Outline each blood parasite and name the species.
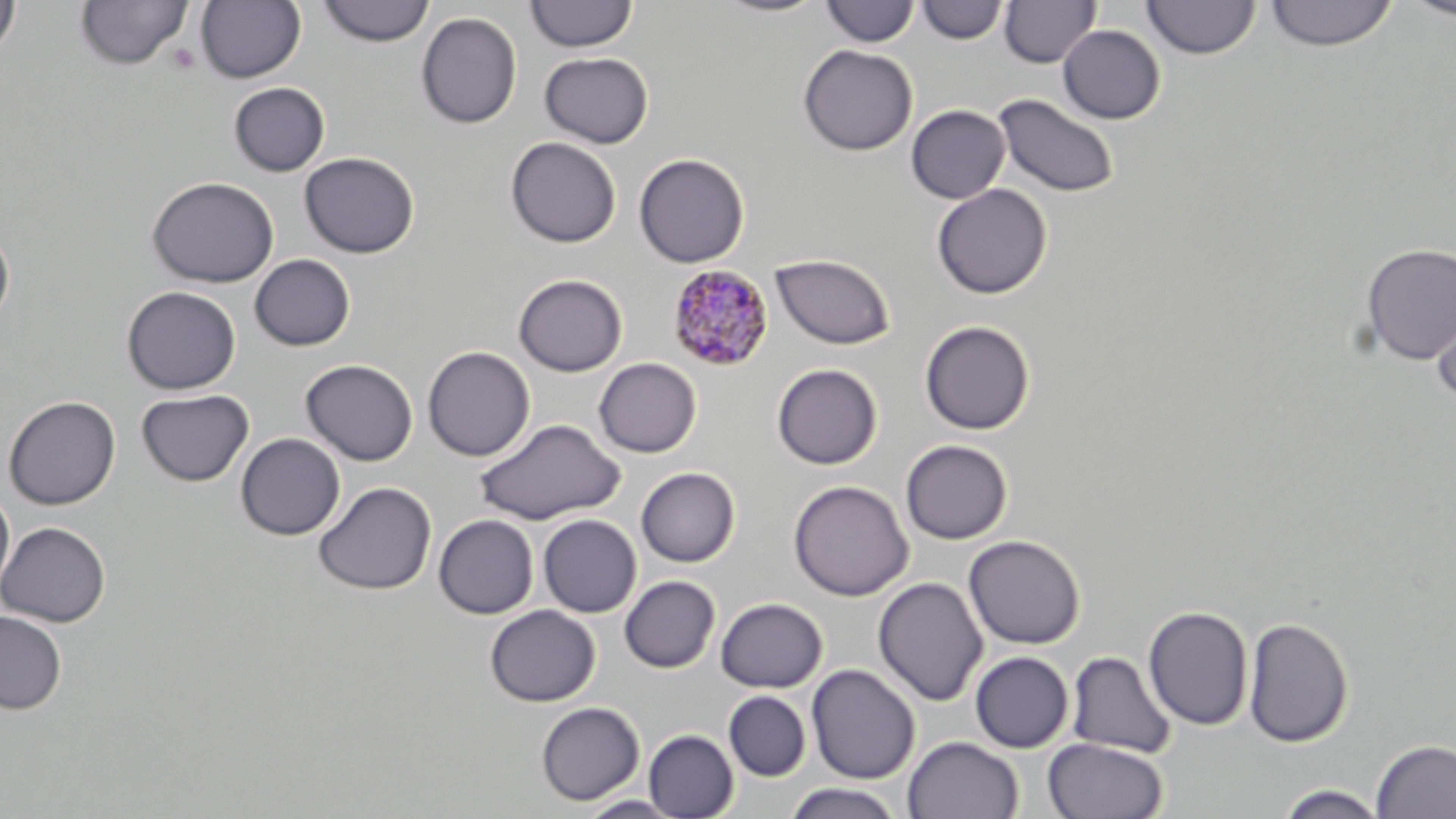

Approximate bounding boxes as named x1/y1/x2/y2 corners in pixels.
Plasmodium malariae-infected red blood cells: (x1=667, y1=263, x2=774, y2=372).
No Plasmodium falciparum, Plasmodium ovale, Plasmodium vivax, Babesia divergens, or Trypanosoma brucei observed.

Summary:
  - Uninfected red blood cell locations: (x1=0, y1=0, x2=21, y2=59), (x1=711, y1=0, x2=830, y2=18), (x1=999, y1=0, x2=1100, y2=68), (x1=1141, y1=0, x2=1261, y2=60), (x1=1265, y1=0, x2=1398, y2=51), (x1=1403, y1=0, x2=1456, y2=21), (x1=74, y1=1, x2=192, y2=70), (x1=196, y1=1, x2=306, y2=83), (x1=318, y1=1, x2=435, y2=47), (x1=524, y1=1, x2=639, y2=52), (x1=820, y1=1, x2=919, y2=47), (x1=916, y1=1, x2=1008, y2=45), (x1=416, y1=12, x2=522, y2=129), (x1=1058, y1=25, x2=1165, y2=124), (x1=798, y1=44, x2=918, y2=156), (x1=539, y1=52, x2=653, y2=148), (x1=228, y1=82, x2=330, y2=176), (x1=993, y1=93, x2=1120, y2=198), (x1=905, y1=104, x2=1010, y2=204), (x1=505, y1=136, x2=621, y2=248), (x1=299, y1=152, x2=420, y2=258), (x1=633, y1=153, x2=750, y2=267), (x1=147, y1=176, x2=279, y2=288), (x1=932, y1=183, x2=1052, y2=299), (x1=0, y1=226, x2=15, y2=327), (x1=1359, y1=242, x2=1456, y2=365), (x1=771, y1=253, x2=896, y2=350), (x1=249, y1=254, x2=355, y2=352), (x1=512, y1=273, x2=628, y2=376), (x1=1430, y1=285, x2=1456, y2=403), (x1=122, y1=286, x2=241, y2=394), (x1=919, y1=320, x2=1036, y2=434), (x1=422, y1=346, x2=535, y2=462), (x1=594, y1=357, x2=702, y2=458), (x1=300, y1=359, x2=418, y2=466), (x1=771, y1=363, x2=882, y2=469), (x1=136, y1=389, x2=253, y2=486), (x1=3, y1=395, x2=121, y2=509), (x1=474, y1=417, x2=625, y2=525), (x1=235, y1=434, x2=345, y2=540), (x1=900, y1=439, x2=1013, y2=545), (x1=635, y1=467, x2=740, y2=567), (x1=788, y1=479, x2=914, y2=601), (x1=312, y1=481, x2=436, y2=595), (x1=0, y1=487, x2=15, y2=599), (x1=538, y1=514, x2=641, y2=617), (x1=434, y1=515, x2=538, y2=619), (x1=0, y1=521, x2=111, y2=627), (x1=963, y1=535, x2=1085, y2=649), (x1=619, y1=575, x2=720, y2=673), (x1=873, y1=576, x2=988, y2=707), (x1=715, y1=597, x2=828, y2=692), (x1=1143, y1=604, x2=1254, y2=732), (x1=485, y1=605, x2=600, y2=707), (x1=0, y1=610, x2=66, y2=714), (x1=1243, y1=616, x2=1354, y2=748), (x1=969, y1=651, x2=1073, y2=753), (x1=1065, y1=651, x2=1176, y2=758), (x1=806, y1=663, x2=921, y2=784), (x1=724, y1=691, x2=811, y2=781), (x1=536, y1=701, x2=645, y2=805), (x1=644, y1=730, x2=738, y2=818), (x1=903, y1=736, x2=1024, y2=819), (x1=1044, y1=737, x2=1168, y2=819), (x1=1371, y1=739, x2=1456, y2=818), (x1=782, y1=783, x2=906, y2=819), (x1=1274, y1=784, x2=1390, y2=819), (x1=575, y1=795, x2=686, y2=819)
  - Slide-level diagnosis: Plasmodium malariae
  - Field of view: one of a larger specimen
  - Modality: light microscopy
  - Preparation: thin blood film
  - Image size: 1456×819 pixels
  - Magnification: 1000x
  - Stain: May-Grünwald-Giemsa